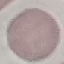
result = negative for malaria parasites
stain = Giemsa
preparation = thin blood smear
capture = smartphone through the microscope eyepiece
image type = cell patch, automatically extracted from a larger field of view and resized to 64 × 64 pixels